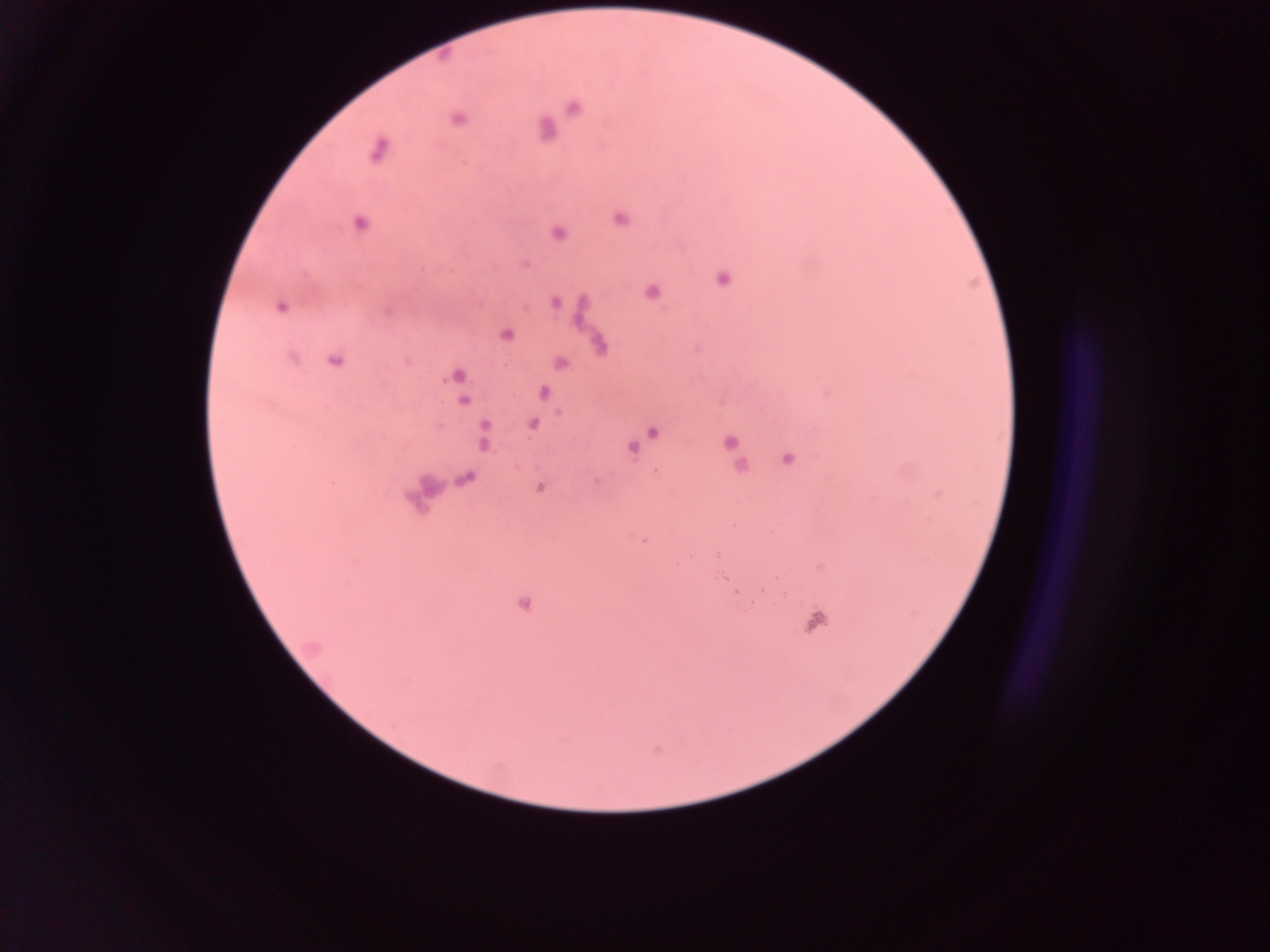

Approximate centers as (x, y) in pixels.
Summary:
  - Malaria parasite locations: (572, 107), (457, 118), (544, 129), (378, 150), (619, 217), (359, 223), (556, 233), (525, 263), (722, 279), (651, 292), (554, 302), (281, 306), (505, 335), (600, 344), (334, 360), (559, 362), (456, 375), (542, 391), (463, 399), (532, 423), (653, 432), (483, 437), (728, 441), (632, 448), (788, 459), (466, 478), (539, 486), (645, 540), (522, 603)
  - Leukocyte locations: (814, 621)
  - Field of view: single
  - Capture: mobile-phone photograph through a microscope
  - Preparation: thick blood film
  - Country: Ghana
  - Image size: 1270×952 pixels